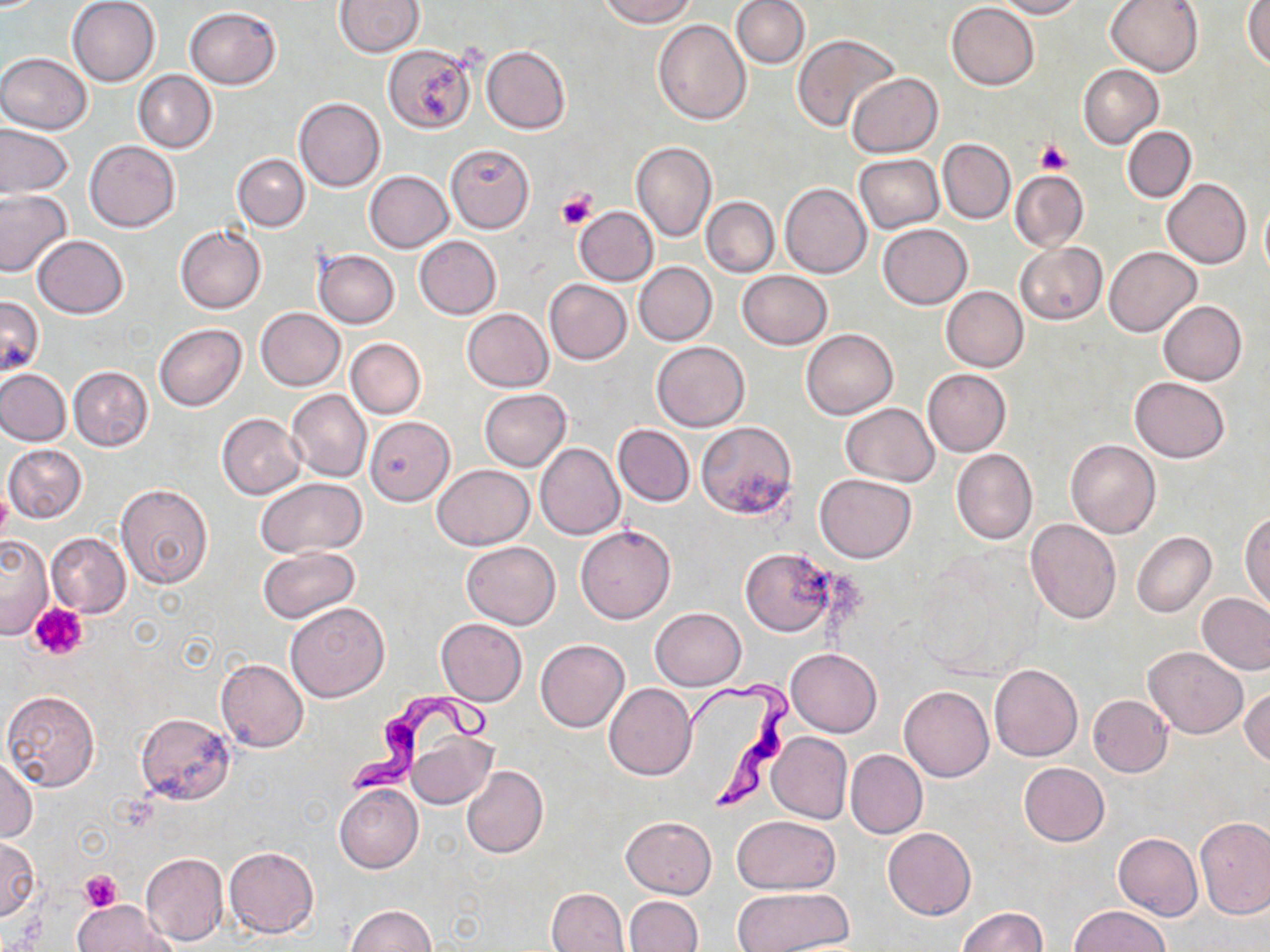

Summary:
  - Coordinate format: approximate bounding boxes as (x1,y1)-(x2,y2) corner pairs in pixels
  - Uninfected red blood cell locations: (67,0)-(161,86), (598,0)-(697,27), (732,0)-(809,69), (993,0)-(1084,18), (1104,0)-(1204,77), (335,1)-(422,57), (946,2)-(1038,90), (1243,2)-(1270,70), (184,6)-(282,90), (654,19)-(751,124), (792,33)-(897,131), (384,43)-(476,133), (481,46)-(571,134), (0,53)-(92,134), (1078,64)-(1163,149), (133,70)-(217,153), (847,73)-(943,157), (294,97)-(385,193), (0,126)-(74,198), (1122,126)-(1196,202), (938,139)-(1015,223), (84,140)-(180,232), (631,142)-(717,244), (445,144)-(535,233), (232,153)-(310,230), (853,154)-(944,232), (1010,169)-(1088,252), (364,171)-(452,253), (1163,179)-(1251,269), (781,183)-(871,279), (0,189)-(73,280), (1259,195)-(1270,281), (701,196)-(779,277), (573,206)-(658,286), (878,223)-(972,309), (176,225)-(266,313), (32,236)-(129,318), (414,236)-(501,319), (1015,243)-(1106,324), (1103,246)-(1199,336), (315,250)-(399,329), (634,262)-(716,345), (737,271)-(833,350), (544,279)-(632,364), (941,287)-(1028,372), (0,294)-(43,377), (1158,301)-(1247,385), (257,308)-(345,389), (462,308)-(553,391), (154,324)-(246,411), (801,328)-(898,419), (346,338)-(426,418), (652,341)-(749,431), (69,366)-(153,451), (0,369)-(70,445), (923,369)-(1011,455), (1129,376)-(1230,463), (286,389)-(371,482), (479,389)-(571,470), (841,403)-(938,486), (217,414)-(307,499), (364,417)-(453,505), (696,421)-(798,520), (614,425)-(694,506), (1066,439)-(1161,538), (535,442)-(624,539), (3,444)-(87,523), (951,450)-(1037,544), (433,464)-(533,549), (814,473)-(916,563), (256,477)-(368,557), (117,484)-(214,588), (1240,512)-(1269,611), (1025,519)-(1121,624), (576,525)-(676,624), (1131,531)-(1216,618), (46,532)-(131,619), (0,534)-(54,639), (462,540)-(560,628), (258,546)-(360,623), (741,546)-(839,636), (1197,593)-(1270,675), (285,601)-(390,702), (651,607)-(745,689), (435,618)-(527,706), (535,640)-(629,732), (1142,646)-(1249,739), (785,648)-(882,737), (215,657)-(309,753), (989,663)-(1082,761), (605,683)-(696,779), (899,686)-(994,781), (1241,688)-(1270,768), (1,690)-(102,793), (1087,694)-(1173,777), (134,713)-(235,804), (405,731)-(496,810), (767,732)-(852,824), (845,750)-(927,840), (0,755)-(38,843), (1018,762)-(1110,847), (462,766)-(548,858), (333,784)-(423,873), (621,815)-(717,898), (732,815)-(840,892), (1195,816)-(1269,917), (883,827)-(975,920), (1113,832)-(1202,921), (0,837)-(41,920), (224,846)-(319,938), (139,852)-(228,945), (547,887)-(629,952), (731,887)-(851,951), (623,896)-(702,952), (71,901)-(175,952), (344,905)-(437,952), (1070,905)-(1169,952), (956,907)-(1048,952)
  - Trypanosoma brucei locations: (684,677)-(792,815), (344,690)-(498,793)
  - Platelet locations: (1036,140)-(1070,176), (555,190)-(598,230), (0,490)-(12,543), (32,604)-(89,659), (79,871)-(122,911)
  - Slide-level diagnosis: Trypanosoma brucei
  - Modality: optical microscopy
  - Field of view: one of a larger specimen
  - Preparation: thin blood film
  - Stain: May-Grünwald-Giemsa
  - Magnification: 1000x
  - Image size: 1270×952 pixels